Describe the morphology of the red blood cells.
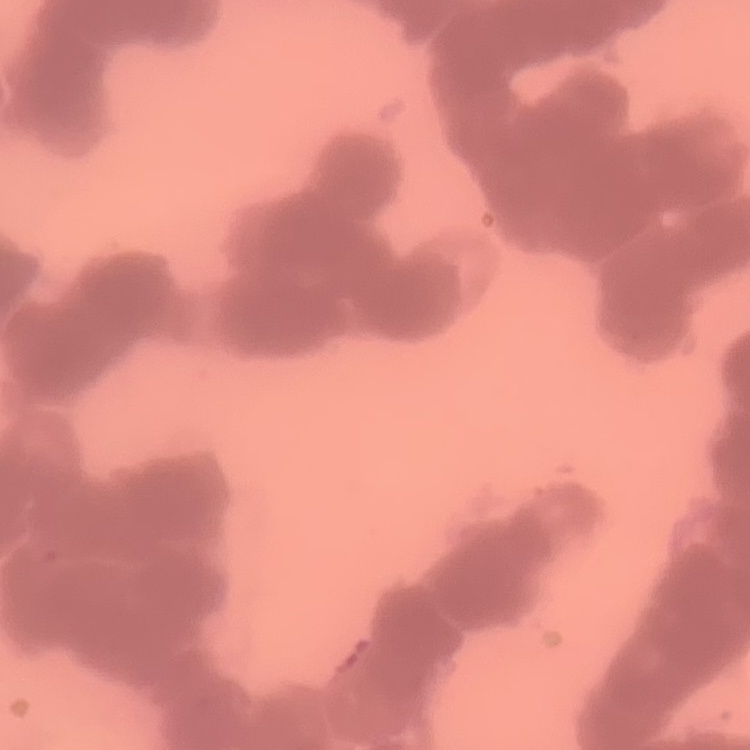
Rouleaux formation.

Thin blood film. Square crop of a larger photomicrograph. Stained with either Field's or Giemsa.